Report the malaria status of this cell.
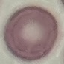

It is uninfected.

stain = Giemsa
capture = smartphone camera at the microscope eyepiece
preparation = thin blood smear
image type = cell patch, automatically extracted from a larger field of view and resized to 64 × 64 pixels